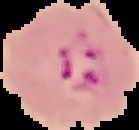

{
  "preparation": "thin blood film",
  "image_type": "segmented cell region with the area outside set to black",
  "result": "Plasmodium parasites detected",
  "image_size": "139×130 pixels"
}